State the preparation type.
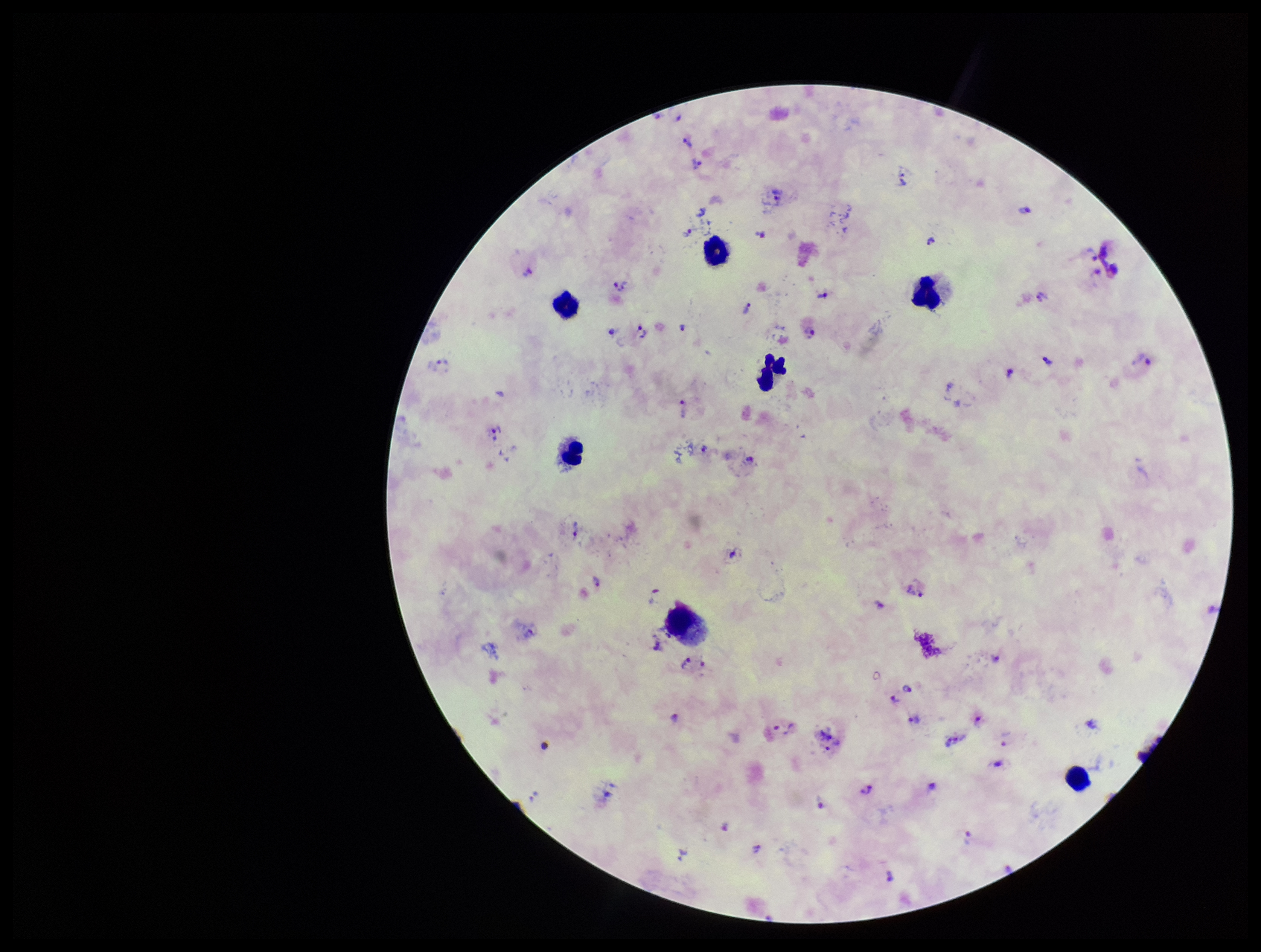
Thick.

Species reported for this patient: Plasmodium vivax. Single field of view. Plasmodium parasites: detected. Photographed through the microscope eyepiece with a smartphone camera. Image is 1261×952 pixels. Leukocyte count: 7. Parasite count: 55. Patient malaria status: positive. Stained with Giemsa.